Outline each blood parasite and name the species.
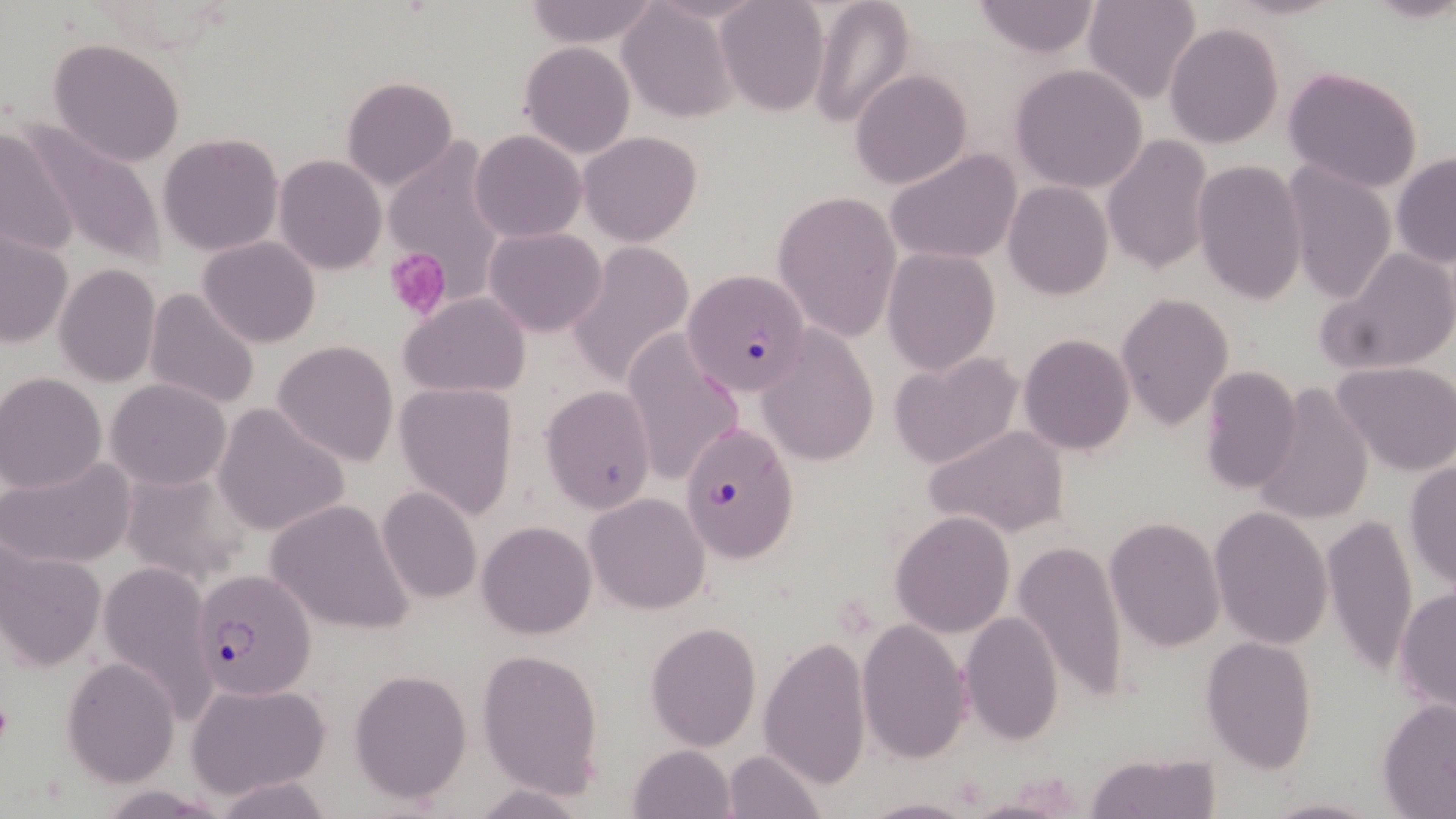

Approximate bounding boxes as (x1,y1)-(x2,y2) corner pairs in pixels.
Plasmodium falciparum-infected red blood cells: (682,268)-(813,396), (679,421)-(799,562), (190,570)-(315,701).
No Plasmodium ovale, Plasmodium malariae, Plasmodium vivax, Babesia divergens, or Trypanosoma brucei observed.

Uninfected red blood cell locations: (520,0)-(663,49), (715,0)-(830,116), (808,0)-(919,129), (971,0)-(1101,59), (1082,0)-(1201,105), (616,3)-(740,124), (1164,22)-(1284,149), (46,38)-(187,169), (519,40)-(635,157), (1011,64)-(1148,193), (1283,65)-(1424,194), (849,69)-(973,190), (341,77)-(457,189), (18,115)-(166,270), (0,125)-(84,262), (470,130)-(587,242), (578,130)-(702,246), (158,132)-(285,257), (1102,135)-(1214,274), (381,139)-(507,305), (886,148)-(1023,265), (1391,153)-(1456,269), (274,154)-(386,275), (1192,160)-(1308,303), (1282,161)-(1398,304), (1004,182)-(1113,301), (772,189)-(903,343), (484,227)-(607,337), (0,229)-(73,349), (198,237)-(320,349), (567,240)-(693,387), (1318,246)-(1456,377), (881,247)-(1000,374), (53,263)-(160,388), (143,286)-(262,413), (399,292)-(531,399), (1116,292)-(1234,430), (1020,314)-(1232,443), (622,328)-(745,489), (758,330)-(880,467), (1017,334)-(1137,456), (274,340)-(399,466), (888,351)-(1024,470), (1332,362)-(1456,475), (1198,365)-(1302,495), (0,372)-(108,494), (107,378)-(230,490), (1252,382)-(1374,524), (394,383)-(517,520), (540,385)-(656,513), (212,406)-(348,535), (922,422)-(1071,539), (1,454)-(138,570), (1403,461)-(1456,591), (375,486)-(484,605), (585,491)-(712,614), (263,501)-(416,635), (1208,505)-(1334,650), (890,511)-(1014,639), (1322,513)-(1417,675), (1104,516)-(1226,652), (477,521)-(596,639), (1013,536)-(1129,708), (1,538)-(106,672), (97,560)-(216,723), (1393,587)-(1456,715), (959,612)-(1065,746), (858,618)-(972,764), (645,622)-(761,750), (758,632)-(871,790), (1199,635)-(1318,772), (475,647)-(604,799), (63,657)-(178,787), (349,669)-(473,803), (189,681)-(333,797), (1379,698)-(1456,817), (628,745)-(735,818), (722,749)-(825,818), (1086,750)-(1221,819), (211,777)-(337,817), (469,783)-(593,818), (1260,794)-(1380,819), (860,795)-(977,819). Platelet locations: (384,248)-(450,320). Slide-level diagnosis: Plasmodium falciparum. Thin blood smear. 1000x magnification. Image is 1456×819 pixels. May-Grünwald-Giemsa-stained preparation. Light microscopy. One field of a larger specimen.